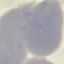 Malaria status: uninfected. Automatically extracted cell patch, resized to 64 × 64 pixels. Thin smear of blood. Giemsa stain. Acquired by smartphone through the microscope eyepiece.